State which parasite is depicted.
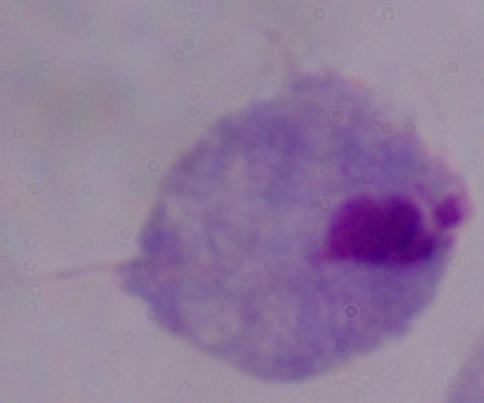

This is a trichomonad.

Summary:
  - Modality: photomicrograph
  - Magnification: 1000x